Assess this cell for malaria.
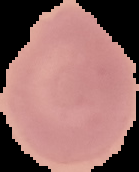

It is uninfected.

Summary:
  - Preparation: thin blood smear
  - Image size: 139×172 pixels
  - Image type: cell region segmented out of the field of view; surrounding area masked to black